State the blood parasite species.
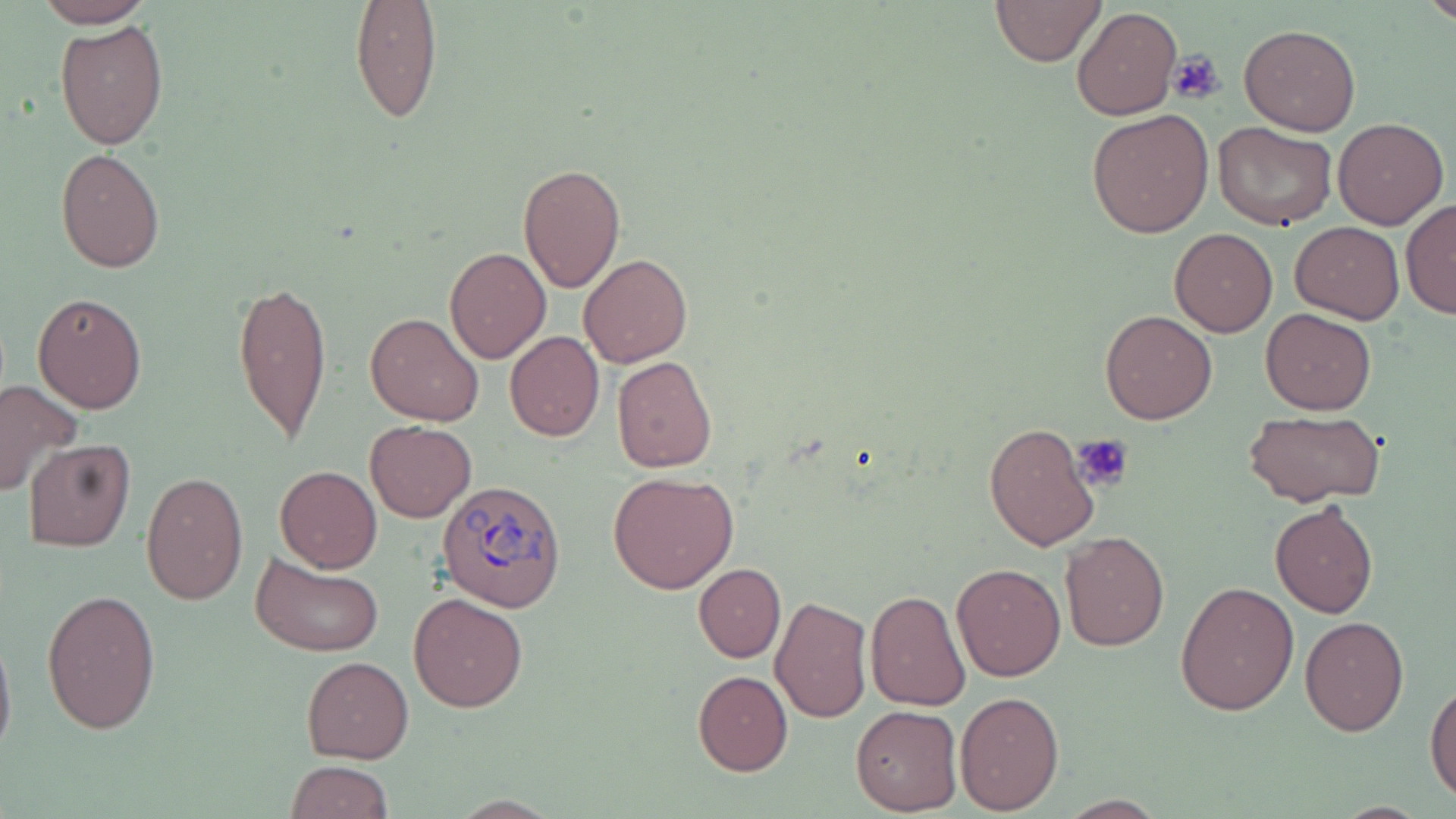
Plasmodium ovale.

Summary:
  - Coordinate format: approximate bounding boxes as named x1/y1/x2/y2 corners in pixels
  - Platelet locations: (x1=1167, y1=51, x2=1224, y2=105), (x1=1073, y1=433, x2=1134, y2=490)
  - Plasmodium ovale-infected red blood cell locations: (x1=437, y1=477, x2=567, y2=611)
  - Uninfected red blood cell locations: (x1=33, y1=0, x2=156, y2=28), (x1=991, y1=0, x2=1106, y2=66), (x1=1421, y1=0, x2=1455, y2=26), (x1=350, y1=1, x2=442, y2=125), (x1=1072, y1=7, x2=1181, y2=121), (x1=55, y1=20, x2=167, y2=150), (x1=1239, y1=23, x2=1360, y2=135), (x1=1086, y1=108, x2=1214, y2=239), (x1=1333, y1=116, x2=1448, y2=229), (x1=1213, y1=122, x2=1337, y2=232), (x1=55, y1=148, x2=165, y2=272), (x1=516, y1=162, x2=626, y2=294), (x1=1401, y1=200, x2=1456, y2=320), (x1=1290, y1=221, x2=1403, y2=322), (x1=1170, y1=228, x2=1277, y2=337), (x1=444, y1=247, x2=551, y2=365), (x1=580, y1=253, x2=692, y2=367), (x1=230, y1=277, x2=332, y2=447), (x1=32, y1=292, x2=148, y2=414), (x1=1259, y1=308, x2=1376, y2=415), (x1=1099, y1=309, x2=1217, y2=424), (x1=365, y1=312, x2=485, y2=426), (x1=505, y1=332, x2=604, y2=442), (x1=611, y1=356, x2=718, y2=473), (x1=0, y1=380, x2=81, y2=499), (x1=1243, y1=409, x2=1386, y2=507), (x1=365, y1=420, x2=477, y2=523), (x1=983, y1=423, x2=1099, y2=550), (x1=23, y1=438, x2=135, y2=552), (x1=273, y1=466, x2=382, y2=573), (x1=609, y1=470, x2=738, y2=593), (x1=138, y1=471, x2=249, y2=606), (x1=1270, y1=500, x2=1378, y2=618), (x1=1059, y1=530, x2=1169, y2=652), (x1=952, y1=550, x2=1168, y2=668), (x1=250, y1=552, x2=384, y2=658), (x1=694, y1=563, x2=785, y2=662), (x1=951, y1=563, x2=1066, y2=681), (x1=1174, y1=581, x2=1299, y2=716), (x1=42, y1=588, x2=161, y2=733), (x1=865, y1=590, x2=970, y2=712), (x1=408, y1=592, x2=528, y2=712), (x1=771, y1=594, x2=871, y2=723), (x1=1300, y1=616, x2=1408, y2=735), (x1=0, y1=625, x2=16, y2=768), (x1=301, y1=656, x2=414, y2=763), (x1=692, y1=670, x2=792, y2=776), (x1=1426, y1=683, x2=1456, y2=804), (x1=956, y1=690, x2=1064, y2=812), (x1=850, y1=705, x2=963, y2=814), (x1=286, y1=760, x2=394, y2=819)
  - Stain: May-Grünwald-Giemsa
  - Magnification: 1000x
  - Field of view: one of a larger specimen
  - Image size: 1456×819 pixels
  - Modality: optical microscopy
  - Preparation: thin blood film